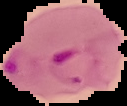
{
  "image_size": "127×106 pixels",
  "preparation": "thin blood smear",
  "image_type": "cell region segmented out of the field of view; surrounding area masked to black",
  "malaria_status": "parasitized"
}